Locate malaria parasites and identify their life-cycle stages.
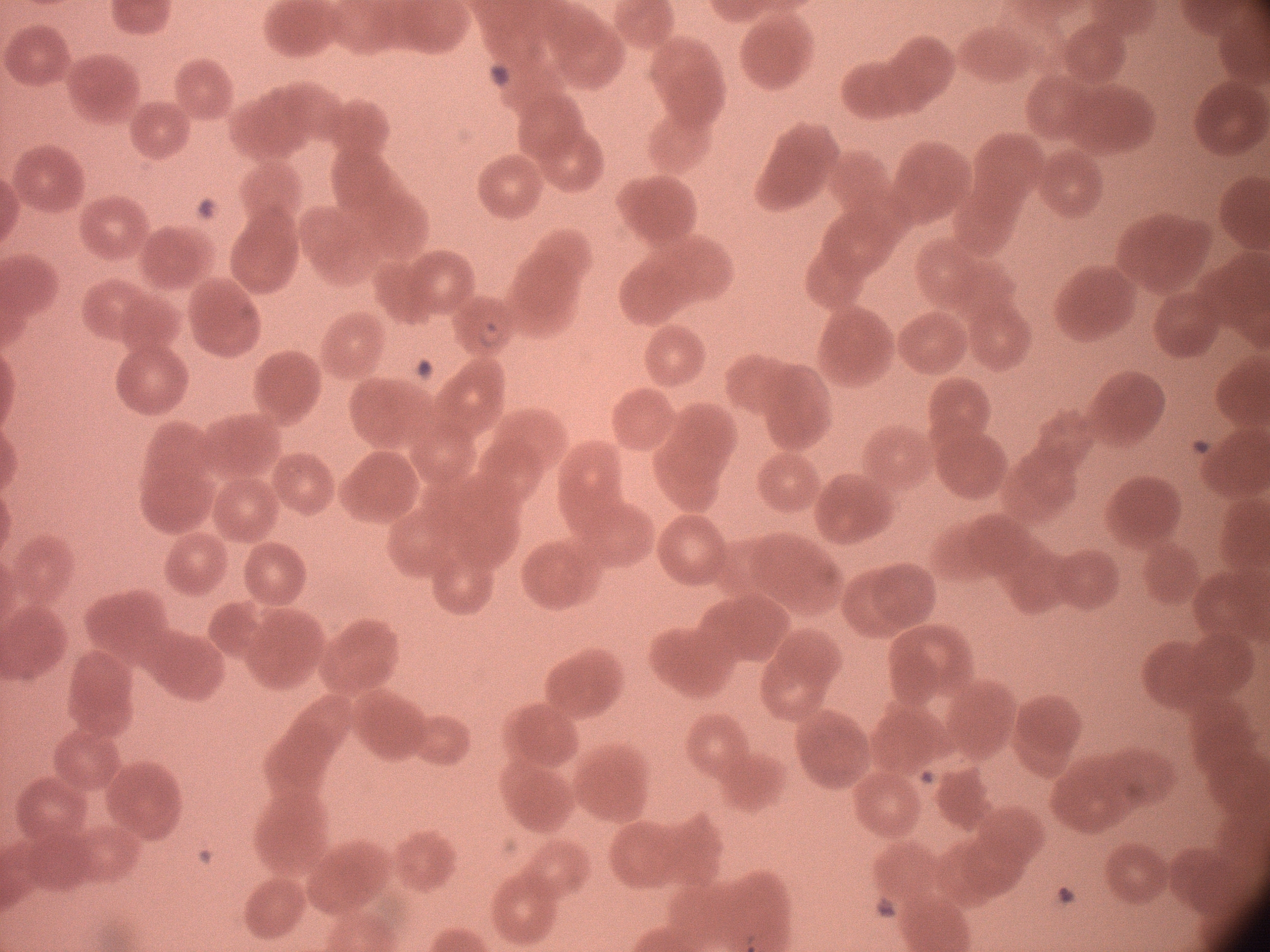
Approximate bounding boxes as [x1, y1, x2, y2] in pixels, from the source annotation, which is not necessarily exhaustive.
Ring forms: [472, 315, 508, 353].

Summary:
  - Species: Plasmodium falciparum
  - Image size: 1270×952 pixels
  - Preparation: thin blood smear
  - Microscope: Leica DM2000 with built-in camera
  - Magnification: 100x
  - Stain: Giemsa
  - Field of view: single